Name the parasite shown.
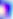
Toxoplasma gondii.

Summary:
  - Magnification: 400x
  - Modality: photomicrograph